Assess the morphology of the red blood cells.
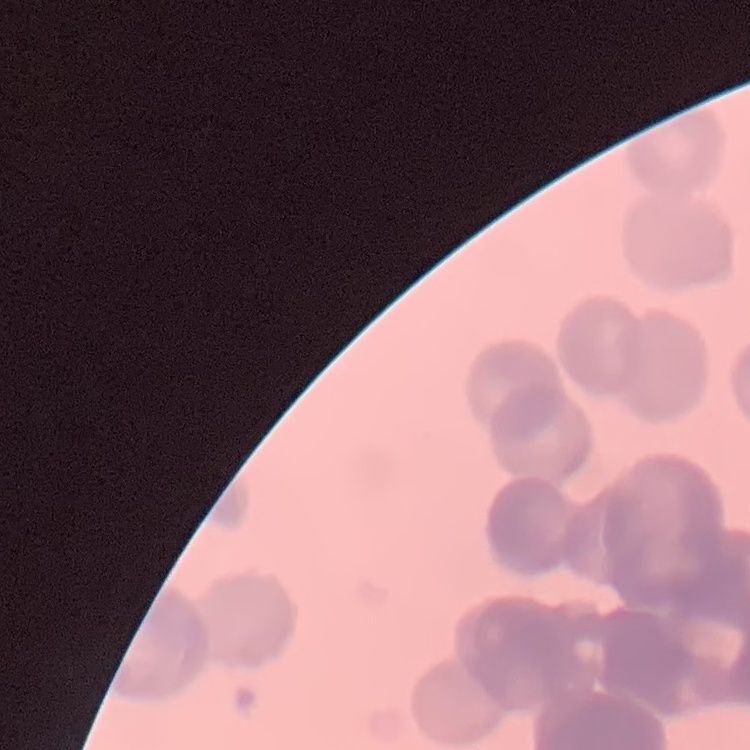

Rouleaux formation.

One tile cut from a larger photomicrograph. Thin blood film. Stained with either Field's or Giemsa.